Assess this cell for malaria.
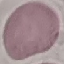
It is uninfected.

preparation = thin blood film
stain = Giemsa
image type = cell patch, automatically extracted from a larger field of view and resized to 64 × 64 pixels
capture = smartphone camera at the microscope eyepiece